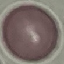

Summary:
  - Result: no malaria parasites seen
  - Stain: Giemsa
  - Image type: automatically extracted cell patch, resized to 64 × 64 pixels
  - Capture: smartphone camera at the microscope eyepiece
  - Preparation: thin smear